Point out each Plasmodium parasite.
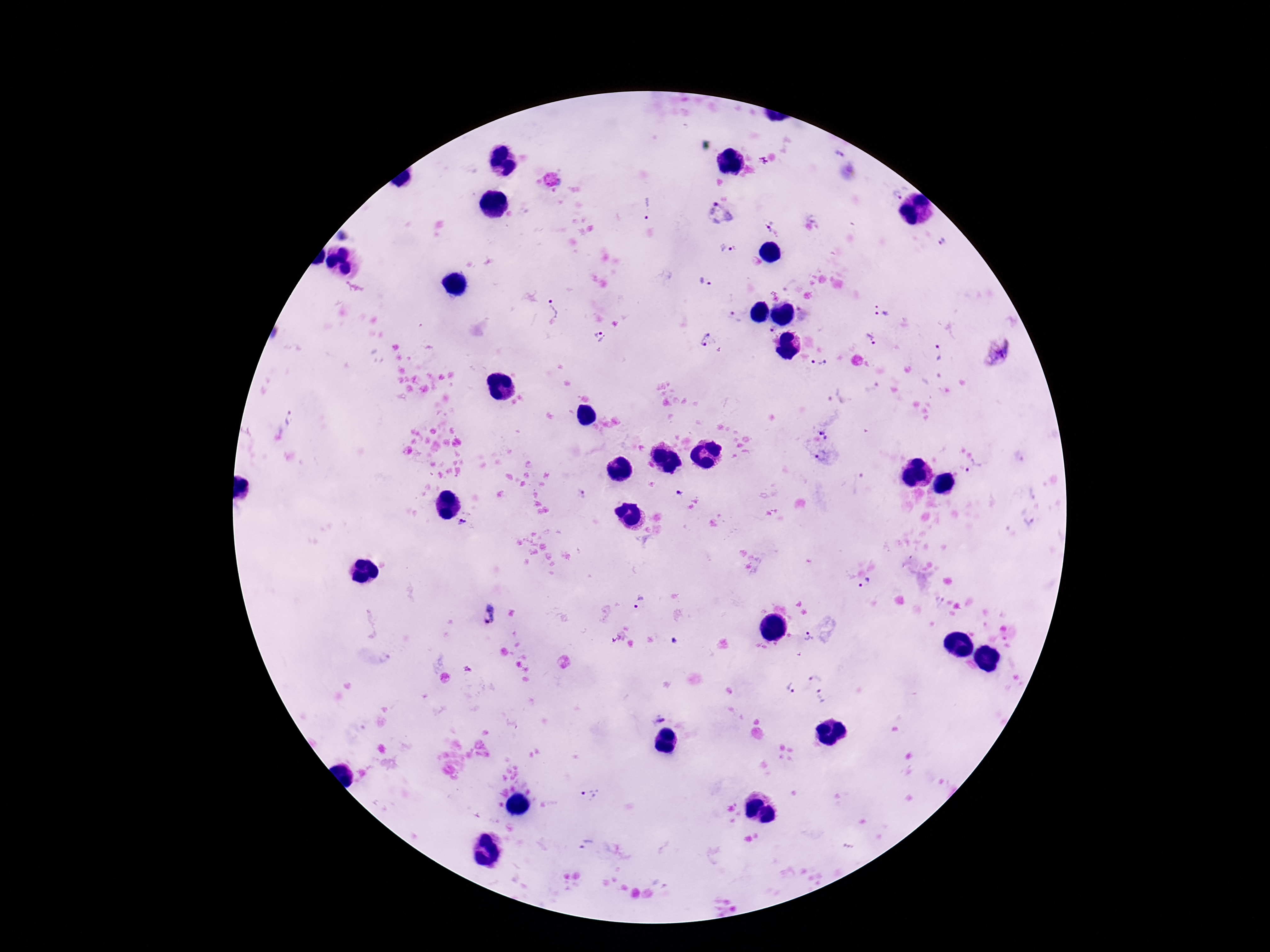
Approximate centers as {x, y} in pixels.
Plasmodium parasites: {838, 154}, {850, 171}, {898, 195}, {647, 209}, {719, 214}, {768, 226}, {344, 236}, {939, 241}, {727, 248}, {705, 282}, {557, 310}, {882, 316}, {733, 319}, {770, 328}, {600, 336}, {871, 338}, {708, 339}, {940, 352}, {995, 353}, {818, 362}, {291, 420}, {826, 431}, {822, 456}, {974, 468}, {679, 493}, {580, 495}, {1031, 521}, {464, 524}, {867, 583}, {640, 603}, {488, 615}, {809, 637}, {676, 641}, {815, 678}, {791, 688}, {821, 697}, {658, 714}, {592, 795}, {584, 842}.

magnification = 100x
image size = 1270×952 pixels
preparation = thick peripheral-blood smear
field of view = one from this slide
stain = Giemsa
capture = smartphone camera through the microscope eyepiece
patient malaria status = infected